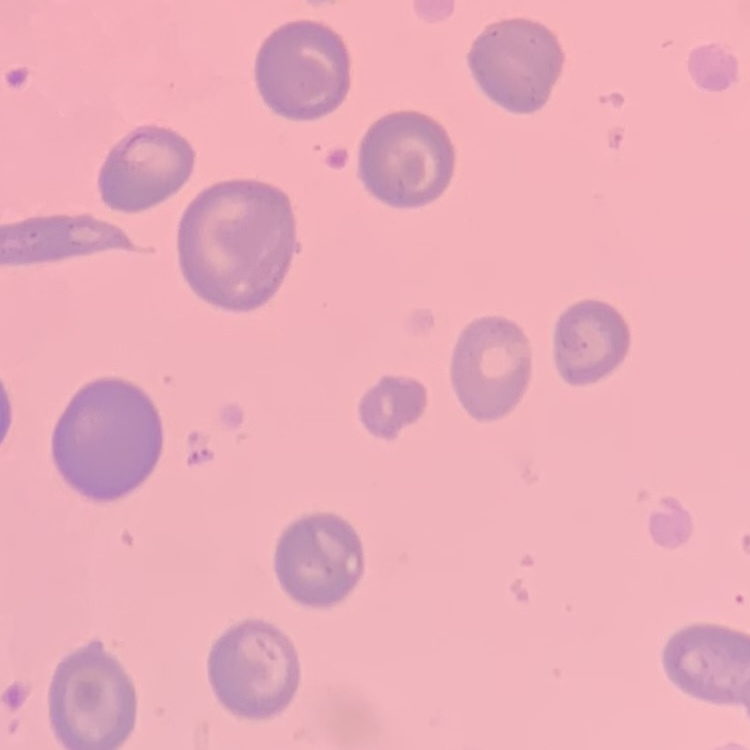

{
  "erythrocyte_morphology": "no rouleaux formation",
  "preparation": "thin blood film",
  "image_type": "one tile cut from a larger photomicrograph",
  "stain": "Field's or Giemsa"
}